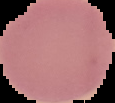

Summary:
  - Preparation: thin blood smear
  - Image type: segmented cell region on a black background
  - Result: negative for Plasmodium parasites
  - Image size: 115×103 pixels